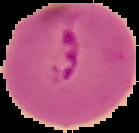
{
  "image_type": "cell region segmented out of the field of view; surrounding area masked to black",
  "malaria_status": "parasitized",
  "image_size": "139×133 pixels",
  "preparation": "thin blood smear"
}